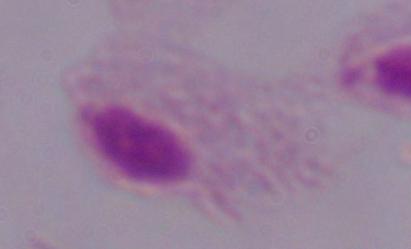
Summary:
  - Magnification: 1000x
  - Identification: trichomonad
  - Modality: micrograph